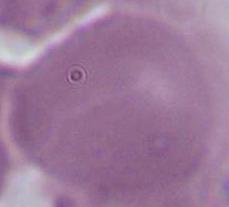

A red blood cell is seen. Captured at 1000x magnification. Photomicrograph.